Locate platelets.
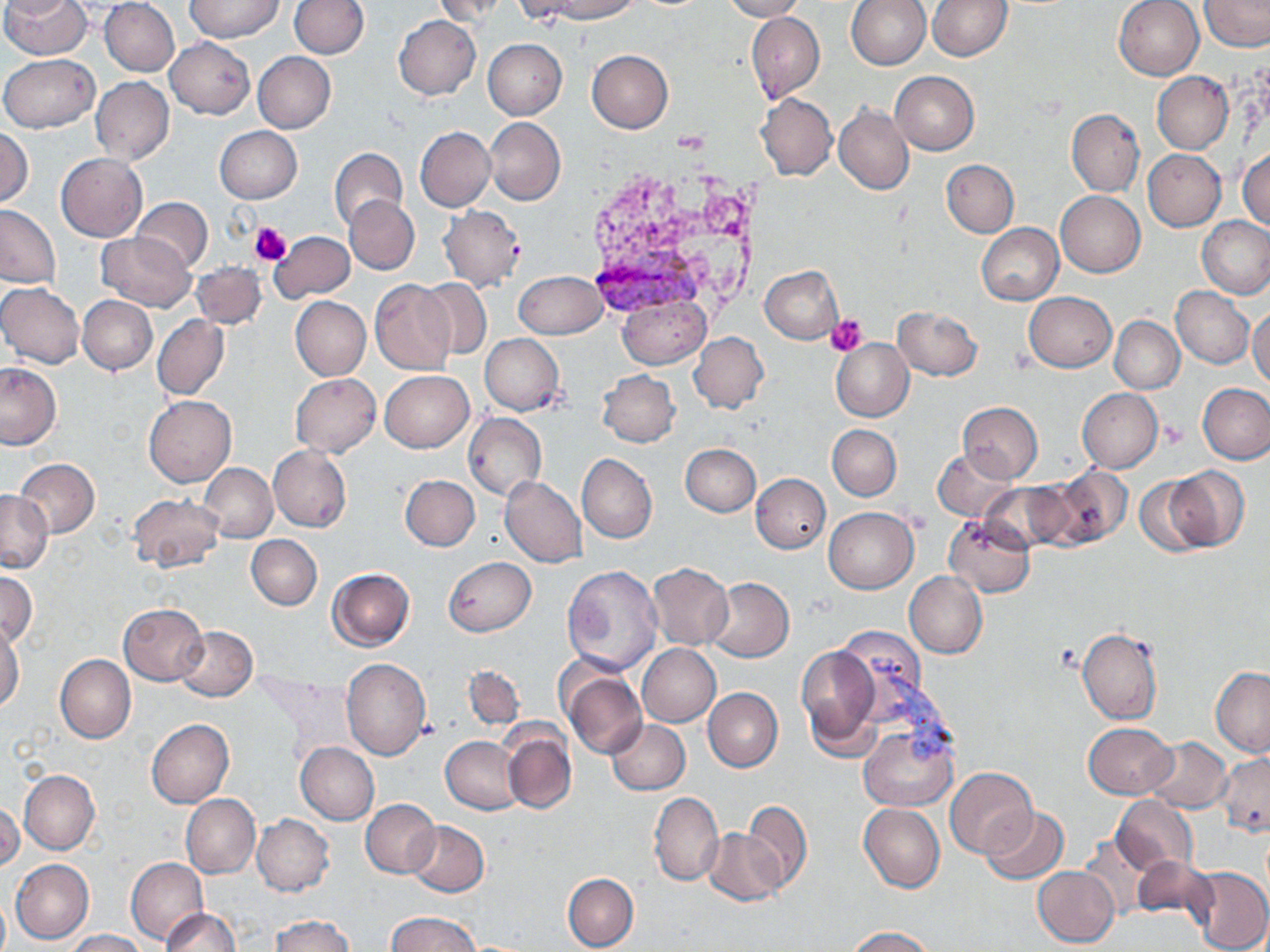

Approximate bounding boxes as [x1, y1, x2, y2] in pixels.
Platelets: [250, 223, 292, 267], [827, 314, 867, 356], [1160, 420, 1187, 445].

Plasmodium vivax-infected red blood cell locations: [579, 231, 716, 320]. Uninfected red blood cell locations: [0, 0, 81, 22], [2, 0, 92, 60], [184, 0, 286, 42], [290, 0, 368, 57], [432, 0, 514, 24], [543, 0, 643, 22], [721, 0, 808, 21], [845, 0, 930, 70], [1114, 0, 1205, 80], [1200, 0, 1269, 52], [100, 1, 179, 76], [927, 1, 1012, 60], [746, 12, 825, 104], [392, 15, 480, 99], [165, 37, 255, 119], [482, 38, 567, 119], [586, 50, 673, 133], [252, 52, 335, 133], [0, 54, 99, 133], [891, 71, 979, 154], [1152, 71, 1233, 153], [91, 77, 174, 164], [756, 92, 837, 181], [834, 104, 914, 195], [1066, 109, 1144, 197], [485, 117, 564, 204], [215, 125, 302, 203], [415, 126, 495, 211], [0, 129, 33, 207], [329, 148, 407, 231], [1238, 148, 1270, 231], [1143, 150, 1225, 230], [55, 153, 146, 241], [941, 159, 1019, 236], [1056, 191, 1144, 277], [345, 196, 418, 274], [131, 197, 212, 273], [0, 204, 60, 288], [438, 205, 526, 292], [1196, 216, 1270, 299], [1186, 218, 1262, 367], [976, 224, 1063, 305], [96, 232, 195, 311], [269, 232, 354, 302], [191, 263, 266, 329], [759, 266, 843, 343], [514, 271, 606, 340], [418, 278, 492, 360], [370, 280, 457, 375], [0, 281, 85, 369], [1170, 286, 1254, 368], [1023, 291, 1116, 371], [77, 295, 157, 375], [617, 296, 710, 369], [290, 297, 370, 380], [1248, 305, 1270, 390], [893, 306, 983, 380], [152, 315, 229, 400], [1110, 316, 1184, 393], [689, 331, 768, 414], [480, 334, 564, 415], [831, 339, 914, 421], [0, 362, 61, 449], [598, 370, 680, 447], [380, 371, 473, 452], [291, 373, 380, 456], [1198, 383, 1270, 464], [1077, 388, 1162, 472], [144, 395, 236, 486], [958, 402, 1042, 482], [464, 412, 546, 501], [827, 425, 901, 500], [679, 444, 760, 516], [268, 445, 352, 532], [933, 449, 1018, 523], [577, 453, 656, 543], [15, 458, 100, 538], [200, 464, 277, 543], [1044, 466, 1132, 549], [1163, 466, 1250, 551], [1133, 472, 1216, 555], [751, 473, 830, 553], [401, 474, 479, 550], [499, 476, 587, 568], [979, 481, 1072, 554], [0, 490, 52, 574], [128, 494, 225, 573], [823, 507, 919, 593], [944, 514, 1034, 596], [246, 535, 321, 610], [442, 557, 536, 636], [646, 563, 734, 651], [562, 566, 662, 675], [327, 567, 414, 650], [903, 571, 988, 658], [1, 572, 36, 647], [706, 577, 794, 662], [118, 604, 208, 685], [0, 621, 24, 712], [174, 626, 257, 699], [836, 626, 927, 715], [1076, 627, 1162, 725], [797, 642, 881, 756], [637, 643, 720, 726], [55, 655, 135, 742], [342, 660, 430, 760], [463, 665, 524, 729], [1210, 666, 1270, 756], [561, 670, 646, 758], [703, 688, 782, 771], [146, 718, 234, 809], [606, 719, 689, 794], [1083, 722, 1176, 798], [860, 727, 957, 810], [502, 728, 575, 813], [441, 736, 524, 814], [1143, 737, 1231, 814], [297, 742, 378, 823], [1216, 753, 1270, 836], [946, 768, 1037, 859], [19, 770, 99, 854], [649, 791, 723, 887], [180, 794, 259, 879], [1111, 795, 1198, 877], [740, 798, 812, 892], [361, 799, 440, 879], [1, 801, 23, 870], [858, 804, 943, 893], [980, 807, 1069, 885], [252, 815, 334, 896], [406, 820, 488, 896], [704, 829, 787, 905], [1079, 835, 1157, 922], [1131, 856, 1218, 927], [126, 858, 208, 945], [10, 859, 93, 945], [1188, 866, 1270, 952], [1033, 867, 1119, 947], [562, 873, 638, 951], [0, 895, 9, 952], [161, 908, 239, 952], [386, 912, 483, 952], [270, 915, 355, 952], [847, 927, 935, 952], [65, 929, 146, 951]. Slide-level diagnosis: Plasmodium vivax. Thin blood film. Single field of view. Image is 1270×952 pixels. Optical microscopy. May-Grünwald-Giemsa stain. 1000x magnification.